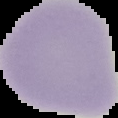

image_size: 118×118 pixels
image_type: segmented cell region with the area outside set to black
preparation: thin blood smear
result: no Plasmodium parasites seen